Name the blood parasite species.
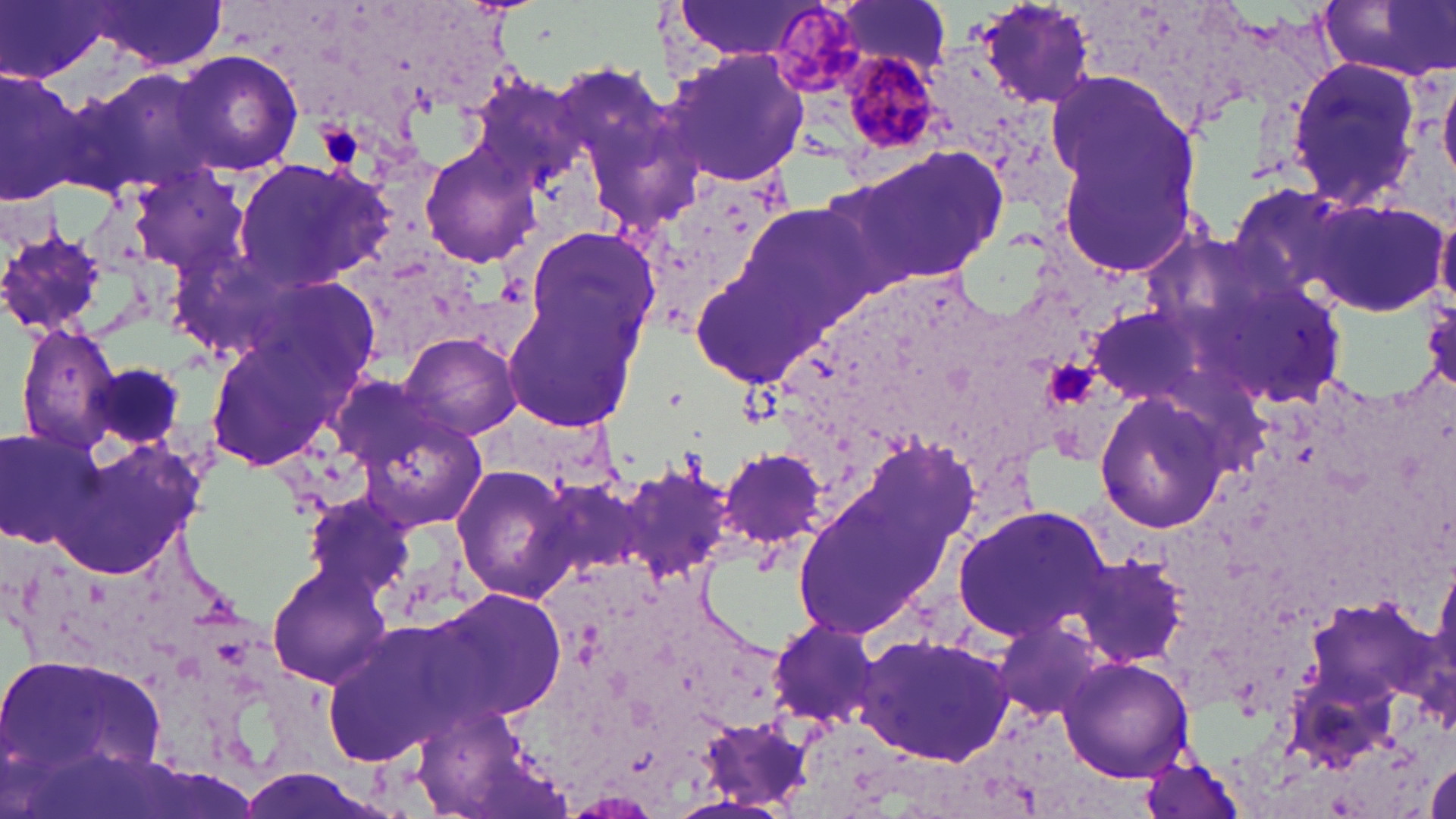

Plasmodium malariae.

Summary:
  - Coordinate format: approximate bounding boxes as named x1/y1/x2/y2 corners in pixels
  - Platelet locations: (x1=320, y1=124, x2=362, y2=167), (x1=1048, y1=358, x2=1094, y2=407)
  - Plasmodium malariae-infected red blood cell locations: (x1=771, y1=6, x2=862, y2=93), (x1=838, y1=49, x2=945, y2=162)
  - Uninfected red blood cell locations: (x1=1, y1=0, x2=111, y2=84), (x1=837, y1=0, x2=951, y2=74), (x1=973, y1=1, x2=1096, y2=113), (x1=1317, y1=1, x2=1455, y2=81), (x1=85, y1=2, x2=227, y2=72), (x1=673, y1=2, x2=821, y2=62), (x1=173, y1=49, x2=303, y2=177), (x1=663, y1=49, x2=812, y2=188), (x1=1286, y1=57, x2=1425, y2=213), (x1=68, y1=64, x2=222, y2=201), (x1=0, y1=65, x2=90, y2=208), (x1=1439, y1=69, x2=1456, y2=184), (x1=1047, y1=70, x2=1208, y2=272), (x1=468, y1=75, x2=587, y2=190), (x1=421, y1=146, x2=539, y2=268), (x1=837, y1=146, x2=1008, y2=291), (x1=232, y1=157, x2=393, y2=291), (x1=132, y1=167, x2=247, y2=273), (x1=631, y1=172, x2=793, y2=336), (x1=1305, y1=200, x2=1446, y2=317), (x1=740, y1=201, x2=884, y2=328), (x1=1436, y1=205, x2=1456, y2=308), (x1=0, y1=225, x2=114, y2=338), (x1=527, y1=225, x2=659, y2=353), (x1=687, y1=245, x2=825, y2=386), (x1=242, y1=272, x2=384, y2=396), (x1=1201, y1=276, x2=1344, y2=405), (x1=504, y1=292, x2=644, y2=428), (x1=1086, y1=305, x2=1210, y2=409), (x1=14, y1=322, x2=120, y2=455), (x1=203, y1=331, x2=353, y2=475), (x1=400, y1=331, x2=523, y2=442), (x1=86, y1=359, x2=189, y2=449), (x1=1093, y1=387, x2=1232, y2=534), (x1=346, y1=395, x2=490, y2=533), (x1=1, y1=427, x2=104, y2=549), (x1=841, y1=434, x2=983, y2=579), (x1=46, y1=435, x2=219, y2=582), (x1=719, y1=446, x2=829, y2=554), (x1=450, y1=463, x2=581, y2=603), (x1=618, y1=464, x2=735, y2=586), (x1=540, y1=473, x2=655, y2=587), (x1=303, y1=495, x2=410, y2=593), (x1=789, y1=498, x2=932, y2=638), (x1=952, y1=504, x2=1107, y2=645), (x1=1073, y1=552, x2=1189, y2=668), (x1=268, y1=564, x2=394, y2=688), (x1=428, y1=589, x2=565, y2=719), (x1=988, y1=614, x2=1111, y2=725), (x1=768, y1=617, x2=882, y2=728), (x1=319, y1=622, x2=474, y2=769), (x1=855, y1=632, x2=1017, y2=766), (x1=4, y1=648, x2=168, y2=798), (x1=1059, y1=657, x2=1194, y2=781), (x1=698, y1=719, x2=813, y2=809), (x1=1139, y1=754, x2=1250, y2=819), (x1=1426, y1=760, x2=1456, y2=818)
  - Field of view: single
  - Preparation: thin blood film
  - Modality: optical microscopy
  - Magnification: 1000x
  - Stain: May-Grünwald-Giemsa
  - Image size: 1456×819 pixels